Name the parasite shown.
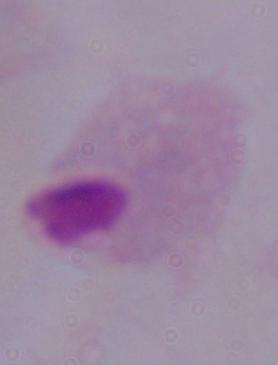

A trichomonad.

modality: photomicrograph
magnification: 1000x